Assess this cell for malaria.
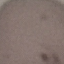

It is uninfected.

Summary:
  - Preparation: thin smear
  - Image type: automatically extracted cell patch, resized to 64 × 64 pixels
  - Stain: Giemsa
  - Capture: smartphone through the microscope eyepiece